Assess this cell for malaria.
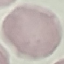
It is uninfected.

Giemsa stain. Cell patch, automatically extracted from a larger field of view and resized to 64 × 64 pixels. Acquired by smartphone through the microscope eyepiece. Thin blood film.